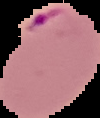
Summary:
  - Preparation: thin blood smear
  - Image size: 100×118 pixels
  - Result: Plasmodium parasites identified
  - Image type: segmented cell region with the area outside set to black